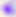
{
  "magnification": "400x",
  "identification": "Toxoplasma gondii",
  "modality": "photomicrograph"
}